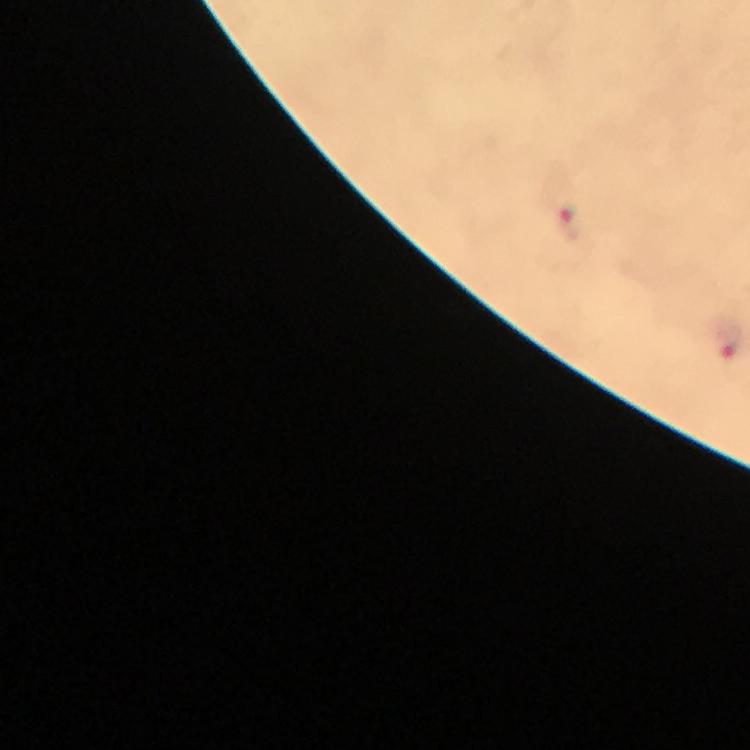
Plasmodium parasite locations = approximate centers as (x, y) in pixels: (571, 224), (728, 341)
immersion oil = used
cropped from = one field of view
context = from a diagnostic examination for malaria
image size = 750×750 pixels
capture = smartphone camera through the microscope
preparation = thick blood film
stain = Giemsa
magnification = 100x